Locate every blood parasite and identify its species.
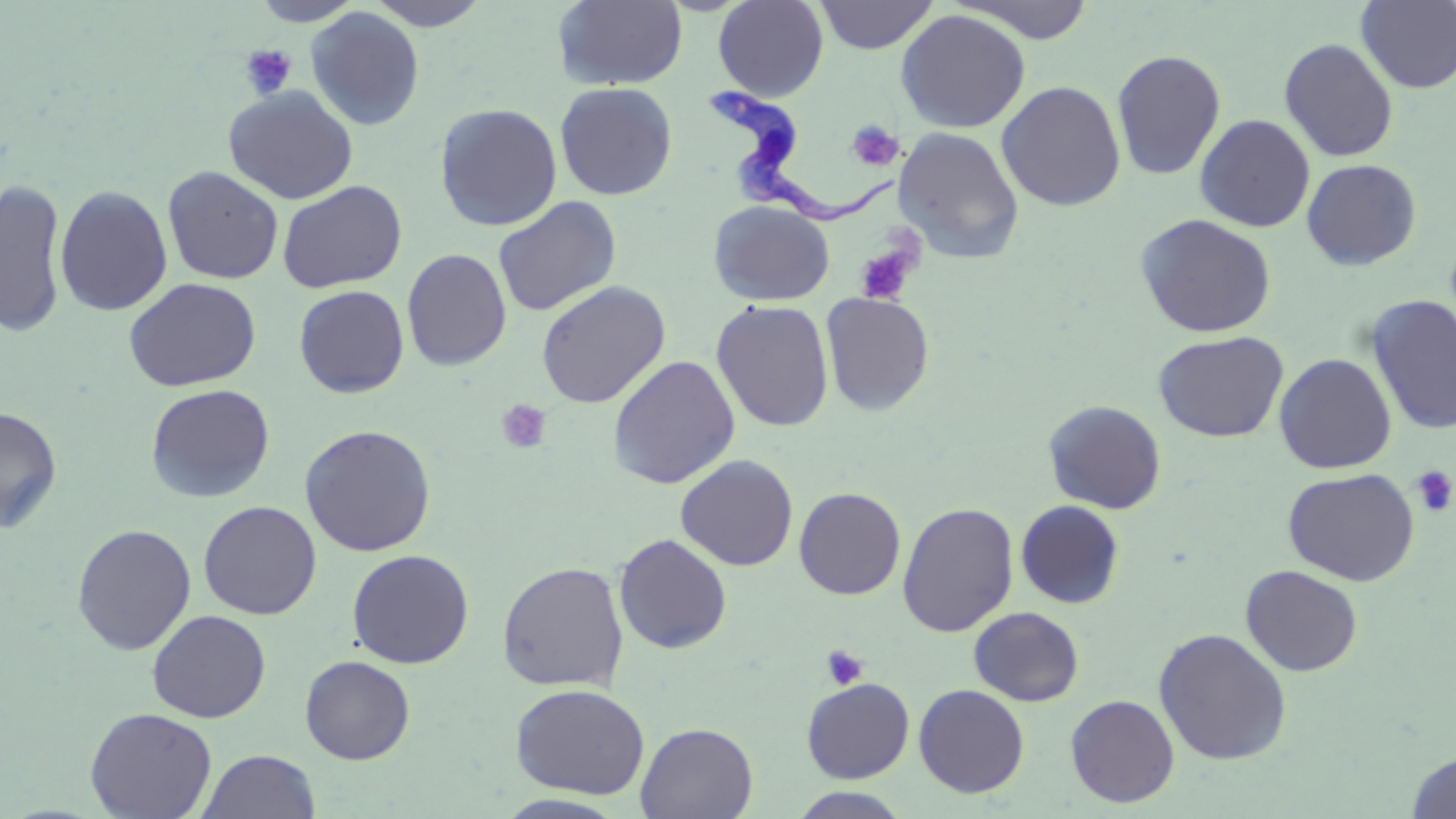
Approximate bounding boxes as (x1,y1)-(x2,y2) corner pairs in pixels.
Trypanosoma brucei: (703,83)-(902,226).
No Plasmodium falciparum, Plasmodium ovale, Plasmodium malariae, Plasmodium vivax, or Babesia divergens observed.

Summary:
  - Platelet locations: (239,44)-(297,99), (845,120)-(904,171), (854,238)-(920,306), (495,400)-(551,454), (1410,465)-(1456,518), (822,645)-(868,690)
  - Uninfected red blood cell locations: (250,0)-(365,26), (365,0)-(494,30), (713,0)-(828,101), (815,0)-(938,54), (949,0)-(1097,43), (554,1)-(688,90), (1355,1)-(1456,93), (305,7)-(425,131), (895,9)-(1031,133), (1279,38)-(1398,162), (1111,49)-(1226,180), (996,80)-(1126,212), (555,82)-(677,200), (223,86)-(359,204), (434,103)-(562,232), (1195,114)-(1315,232), (892,127)-(1025,263), (1302,159)-(1421,270), (162,165)-(284,284), (0,177)-(69,339), (277,180)-(407,293), (54,185)-(173,316), (493,196)-(621,317), (709,200)-(836,306), (1135,213)-(1276,338), (402,248)-(512,371), (124,277)-(261,392), (536,281)-(670,409), (293,285)-(409,398), (821,293)-(935,416), (1366,295)-(1456,435), (711,299)-(834,432), (1153,330)-(1288,442), (1274,353)-(1397,474), (607,355)-(741,490), (145,383)-(275,504), (1043,399)-(1167,514), (0,405)-(63,534), (299,424)-(436,556), (675,455)-(799,572), (1282,467)-(1420,586), (794,487)-(906,600), (198,500)-(322,619), (1015,500)-(1125,609), (897,502)-(1018,637), (71,524)-(196,655), (614,533)-(732,654), (347,549)-(474,669), (496,561)-(629,692), (1240,564)-(1363,676), (968,607)-(1084,707), (147,609)-(271,722), (1153,627)-(1292,765), (300,655)-(415,765), (801,677)-(914,783), (510,683)-(650,799), (913,683)-(1029,798), (1065,694)-(1180,808), (84,706)-(217,819), (635,722)-(758,818), (197,749)-(321,819), (1405,751)-(1456,818), (788,788)-(915,818), (492,793)-(630,818)
  - Slide-level diagnosis: Trypanosoma brucei
  - Stain: May-Grünwald-Giemsa
  - Preparation: thin blood film
  - Magnification: 1000x
  - Modality: optical microscopy
  - Field of view: one of a larger specimen
  - Image size: 1456×819 pixels